Report the malaria status.
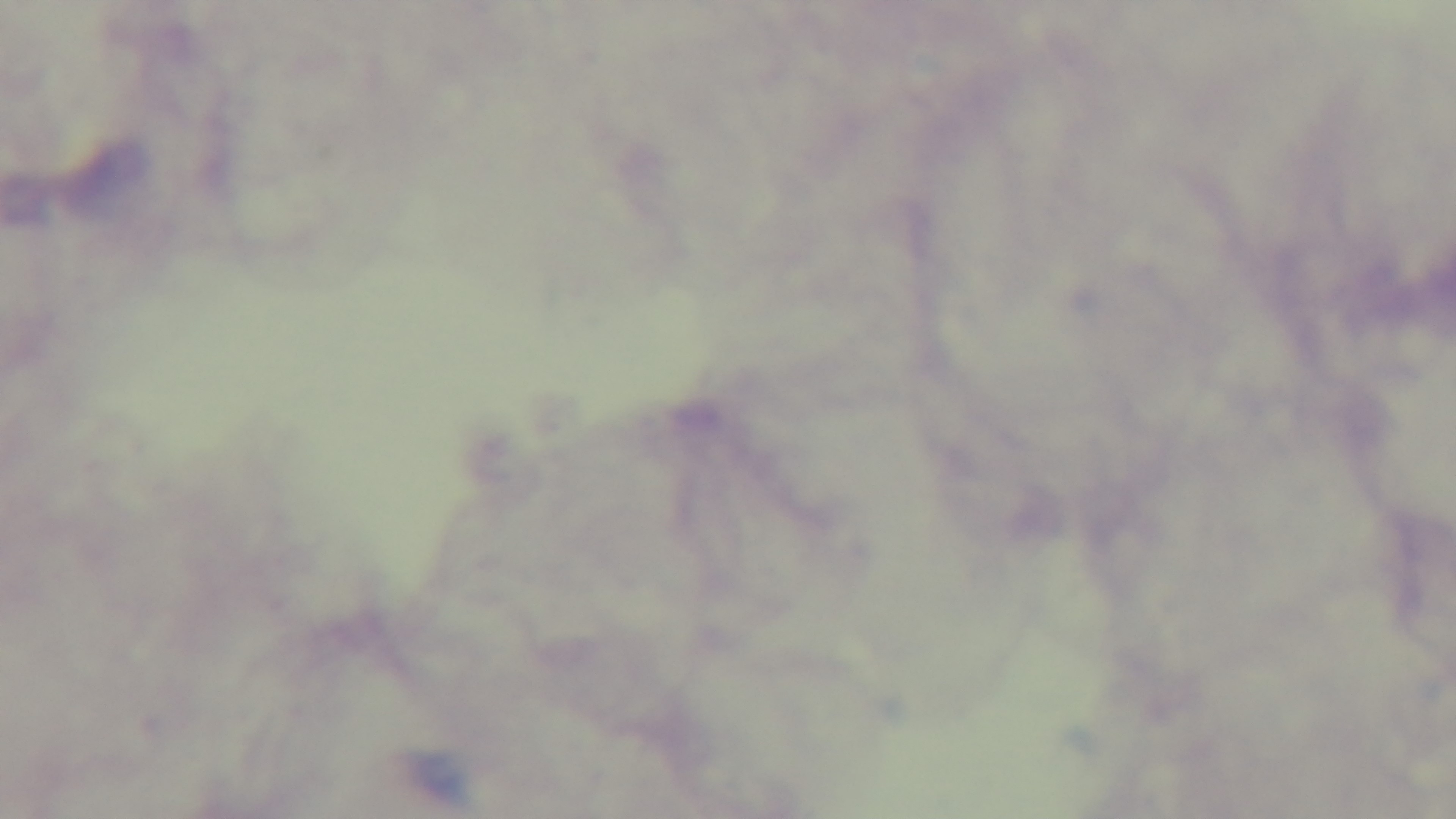
Negative.

modality = light microscopy
objective = 100x oil immersion
preparation = thick blood film
stain = Giemsa
capture = mounted 4K digital camera
field of view = single